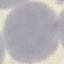

result = no malaria parasites seen
preparation = thin blood smear
image type = automatically extracted cell patch, resized to 64 × 64 pixels
stain = Giemsa
capture = smartphone through the microscope eyepiece